Locate every blood parasite and identify its species.
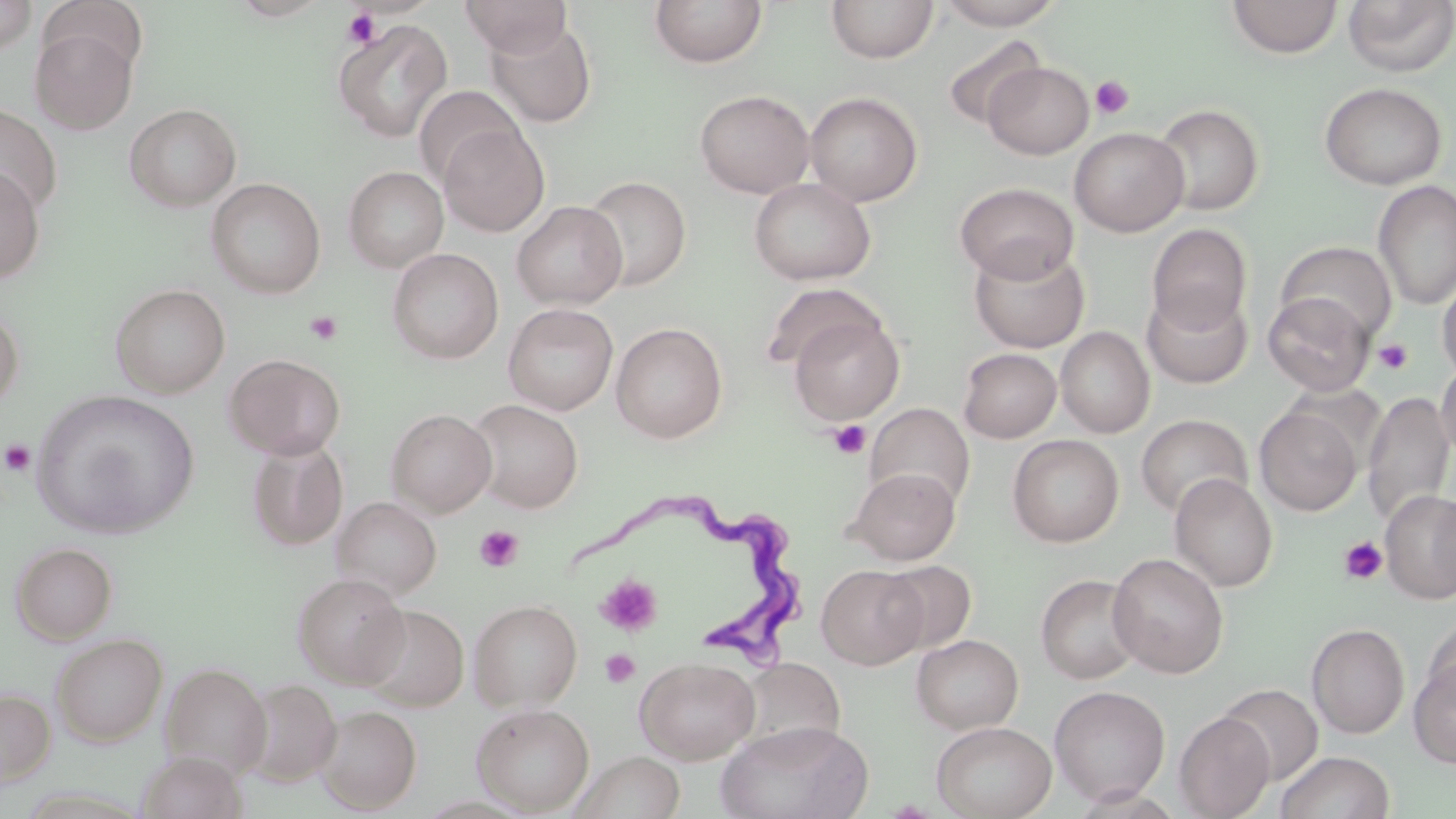
Approximate bounding boxes as named x1/y1/x2/y2 corners in pixels.
Trypanosoma brucei: (x1=564, y1=497, x2=816, y2=670).
No Plasmodium falciparum, Plasmodium ovale, Plasmodium malariae, Plasmodium vivax, or Babesia divergens observed.

slide-level diagnosis = Trypanosoma brucei
preparation = thin blood smear
magnification = 1000x
stain = May-Grünwald-Giemsa
platelet locations = approximate bounding boxes as named x1/y1/x2/y2 corners in pixels: (x1=342, y1=8, x2=382, y2=49), (x1=1090, y1=75, x2=1134, y2=120), (x1=305, y1=311, x2=342, y2=345), (x1=1373, y1=338, x2=1414, y2=374), (x1=827, y1=419, x2=871, y2=460), (x1=1, y1=440, x2=36, y2=477), (x1=474, y1=524, x2=523, y2=571), (x1=1338, y1=536, x2=1388, y2=585), (x1=595, y1=574, x2=663, y2=637), (x1=600, y1=649, x2=640, y2=689)
field of view = single
modality = light microscopy
uninfected red blood cell locations = approximate bounding boxes as named x1/y1/x2/y2 corners in pixels: (x1=0, y1=0, x2=36, y2=55), (x1=460, y1=0, x2=572, y2=58), (x1=649, y1=0, x2=768, y2=69), (x1=936, y1=0, x2=1064, y2=30), (x1=1226, y1=0, x2=1344, y2=59), (x1=1342, y1=0, x2=1456, y2=76), (x1=40, y1=1, x2=149, y2=79), (x1=826, y1=1, x2=939, y2=64), (x1=485, y1=17, x2=597, y2=128), (x1=333, y1=20, x2=452, y2=142), (x1=30, y1=27, x2=137, y2=134), (x1=941, y1=34, x2=1047, y2=131), (x1=983, y1=61, x2=1093, y2=159), (x1=1318, y1=81, x2=1448, y2=189), (x1=414, y1=85, x2=524, y2=188), (x1=695, y1=89, x2=815, y2=198), (x1=804, y1=91, x2=923, y2=206), (x1=0, y1=103, x2=62, y2=216), (x1=125, y1=103, x2=241, y2=212), (x1=1152, y1=103, x2=1264, y2=216), (x1=438, y1=123, x2=549, y2=237), (x1=1069, y1=126, x2=1190, y2=236), (x1=0, y1=165, x2=45, y2=283), (x1=343, y1=165, x2=448, y2=272), (x1=582, y1=175, x2=691, y2=291), (x1=207, y1=178, x2=326, y2=299), (x1=749, y1=178, x2=876, y2=286), (x1=1373, y1=180, x2=1456, y2=310), (x1=954, y1=182, x2=1079, y2=283), (x1=511, y1=201, x2=627, y2=309), (x1=1147, y1=223, x2=1253, y2=335), (x1=1275, y1=240, x2=1398, y2=342), (x1=968, y1=243, x2=1090, y2=353), (x1=387, y1=248, x2=503, y2=364), (x1=1437, y1=268, x2=1456, y2=386), (x1=760, y1=282, x2=884, y2=374), (x1=110, y1=284, x2=230, y2=398), (x1=1142, y1=289, x2=1253, y2=389), (x1=1263, y1=291, x2=1375, y2=396), (x1=503, y1=303, x2=619, y2=415), (x1=0, y1=306, x2=23, y2=414), (x1=788, y1=313, x2=905, y2=425), (x1=610, y1=322, x2=728, y2=443), (x1=1055, y1=326, x2=1155, y2=438), (x1=958, y1=347, x2=1061, y2=443), (x1=224, y1=353, x2=346, y2=460), (x1=1436, y1=358, x2=1456, y2=464), (x1=32, y1=389, x2=199, y2=539), (x1=1362, y1=390, x2=1454, y2=529), (x1=466, y1=399, x2=584, y2=512), (x1=864, y1=402, x2=976, y2=511), (x1=1254, y1=404, x2=1363, y2=516), (x1=386, y1=408, x2=497, y2=516), (x1=1135, y1=414, x2=1253, y2=518), (x1=1007, y1=434, x2=1124, y2=547), (x1=245, y1=438, x2=348, y2=551), (x1=846, y1=467, x2=961, y2=565), (x1=1169, y1=472, x2=1278, y2=591), (x1=1380, y1=489, x2=1456, y2=604), (x1=1434, y1=489, x2=1455, y2=599), (x1=331, y1=496, x2=441, y2=599), (x1=11, y1=542, x2=117, y2=644), (x1=1107, y1=552, x2=1229, y2=678), (x1=879, y1=560, x2=977, y2=654), (x1=815, y1=565, x2=928, y2=669), (x1=292, y1=572, x2=409, y2=688), (x1=1036, y1=573, x2=1144, y2=684), (x1=469, y1=599, x2=583, y2=711), (x1=358, y1=604, x2=469, y2=711), (x1=1422, y1=620, x2=1456, y2=714), (x1=1306, y1=623, x2=1410, y2=738), (x1=51, y1=633, x2=167, y2=746), (x1=912, y1=634, x2=1023, y2=734), (x1=634, y1=656, x2=760, y2=765), (x1=1408, y1=656, x2=1456, y2=769), (x1=739, y1=657, x2=844, y2=754), (x1=161, y1=663, x2=272, y2=777), (x1=240, y1=679, x2=341, y2=786), (x1=1217, y1=683, x2=1324, y2=785), (x1=1049, y1=685, x2=1170, y2=805), (x1=0, y1=688, x2=55, y2=786), (x1=471, y1=703, x2=595, y2=814), (x1=316, y1=704, x2=421, y2=814), (x1=935, y1=710, x2=1171, y2=812), (x1=1174, y1=711, x2=1275, y2=819), (x1=716, y1=720, x2=873, y2=819), (x1=932, y1=721, x2=1056, y2=819), (x1=573, y1=750, x2=686, y2=818), (x1=1275, y1=750, x2=1394, y2=819), (x1=136, y1=751, x2=247, y2=819)
image size = 1456×819 pixels